Locate malaria parasites and leukocytes.
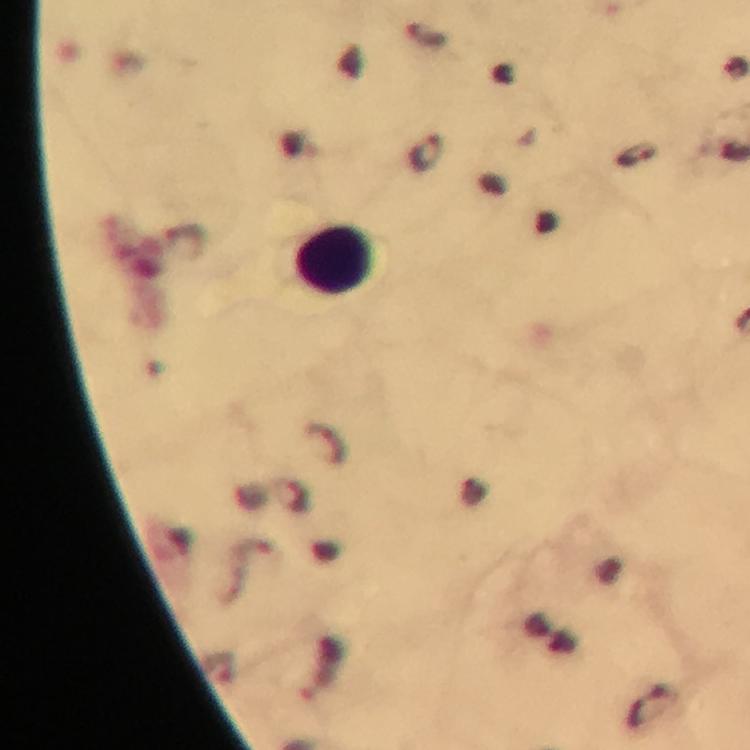

Approximate centers as {x, y} in pixels.
Malaria parasites: {429, 154}, {634, 155}.
Leukocytes: {334, 259}.

preparation = thick blood smear
immersion oil = used
image size = 750×750 pixels
capture = smartphone photograph through a microscope
magnification = 100x
context = from a malaria diagnostic workup
stain = Giemsa
cropped from = one field of view